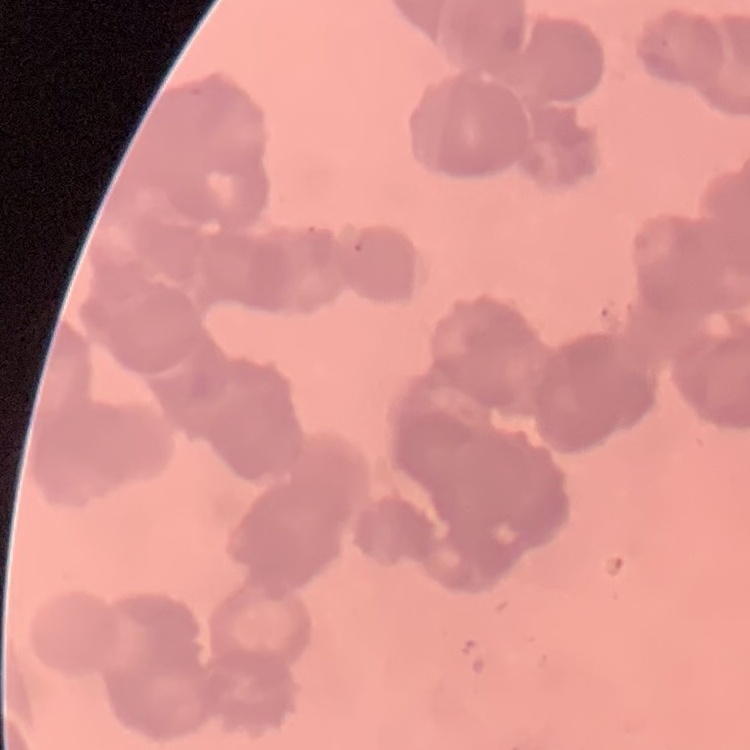
The erythrocytes exhibit rouleaux formation. Thin blood film. Field's or Giemsa stain. One tile cut from a larger photomicrograph.